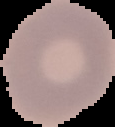

From a thin blood film. Image is 115×127 pixels. Segmented cell region on a black background. Result: negative for malaria parasites.